Report the malaria status of this cell.
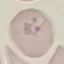
Parasitized.

Cell patch, automatically extracted from a larger field of view and resized to 64 × 64 pixels. Giemsa-stained preparation. Thin blood smear. Acquired by smartphone through the microscope eyepiece.